Locate the cells, classifying each as a parasitized red blood cell, an uninfected red blood cell, or a white blood cell.
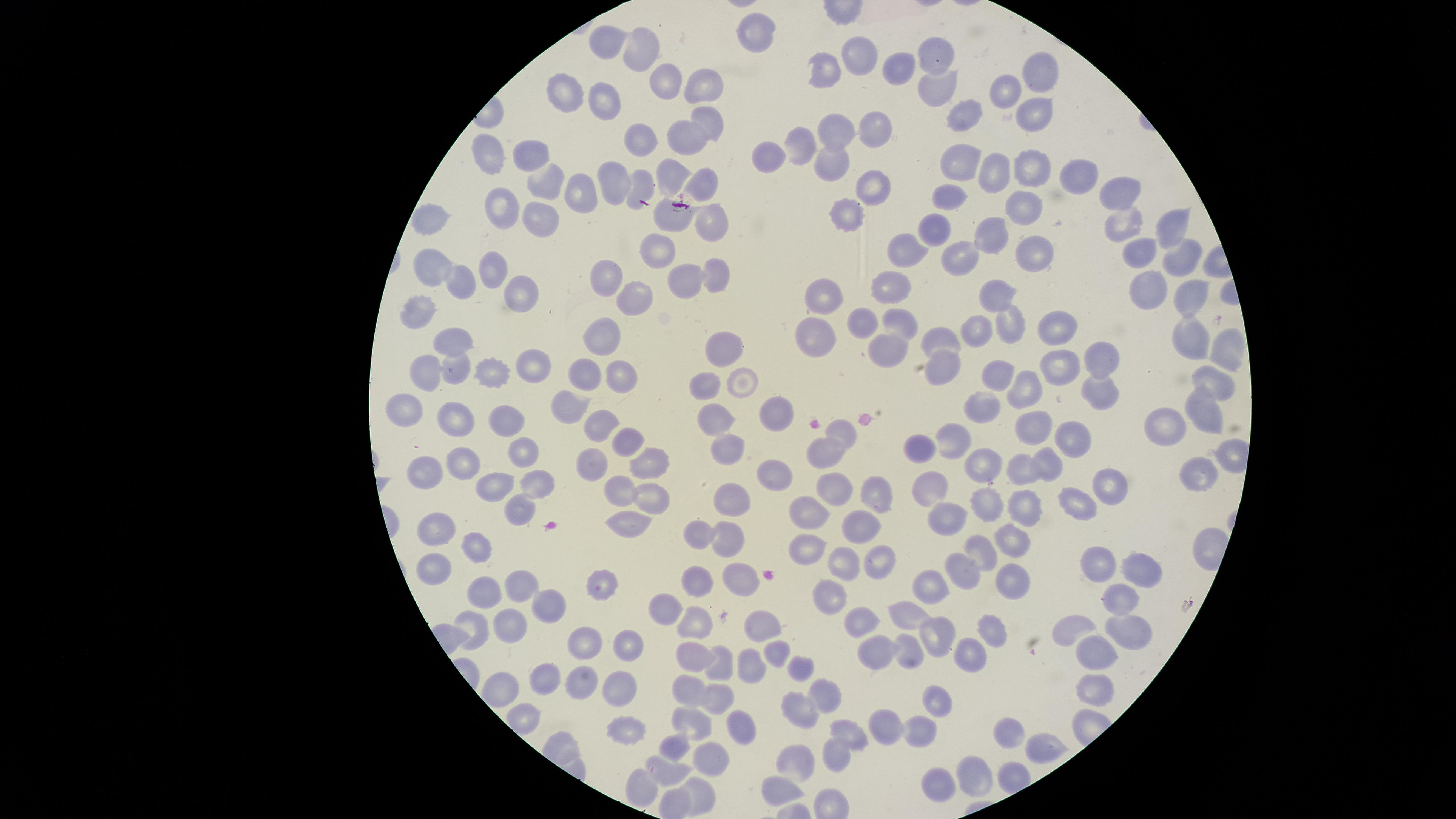
No parasitized red blood cells identified.
Approximate marker points as [x, y] in pixels.
Uninfected red blood cells: [756, 32], [607, 42], [639, 52], [856, 55], [933, 59], [893, 68], [827, 70], [1039, 74], [667, 79], [705, 82], [937, 92], [567, 93], [1003, 93], [599, 105], [1030, 108], [961, 114], [706, 120], [839, 129], [874, 130], [688, 135], [642, 136], [804, 144], [772, 153], [493, 157], [831, 158], [965, 158], [535, 159], [1028, 167], [992, 171], [1071, 172], [618, 174], [672, 174], [547, 184], [702, 184], [873, 184], [639, 185], [1114, 191], [950, 193], [580, 194], [504, 205], [1021, 207], [672, 216], [849, 216], [705, 220], [430, 222], [1123, 222], [541, 224], [1163, 225], [932, 228], [992, 233], [661, 247], [1035, 250], [910, 252], [1142, 253], [959, 259], [1182, 259], [437, 270], [495, 272], [608, 274], [710, 276], [680, 282], [893, 284], [465, 287], [1151, 287], [519, 291], [825, 297], [990, 298], [1187, 298], [636, 302], [421, 315], [866, 322], [902, 322], [1004, 323], [1054, 328], [979, 329], [819, 333], [942, 334], [602, 336], [1193, 338], [448, 340], [720, 342], [1222, 347], [887, 350], [533, 364], [947, 364], [1103, 364], [1053, 365], [452, 368], [426, 371], [622, 374], [490, 375], [582, 375], [996, 376], [1215, 378], [706, 384], [747, 385], [1024, 393], [1099, 394], [984, 399], [569, 406], [411, 409], [1202, 412], [781, 413], [456, 416], [512, 419], [1040, 423], [719, 424], [603, 427], [1165, 427], [844, 429], [626, 436], [1071, 436], [955, 438], [918, 444], [727, 447], [823, 448], [522, 456], [654, 458], [1047, 461], [463, 464], [588, 464], [980, 466], [1025, 469], [1200, 469], [425, 470], [768, 477], [534, 481], [835, 485], [934, 486], [502, 488], [622, 491], [1104, 491], [730, 493], [876, 494], [981, 498], [645, 499], [1024, 503], [1071, 503], [803, 511], [517, 514], [949, 523], [861, 524], [705, 526], [631, 527], [430, 530], [730, 535], [1014, 539], [472, 546], [981, 548], [809, 549], [845, 555], [883, 556], [1099, 561], [1139, 568], [439, 569], [960, 569], [738, 574], [1012, 575], [695, 581], [931, 582], [606, 584], [525, 589], [489, 594], [827, 594], [1119, 599], [666, 605], [548, 607], [912, 614], [864, 617], [759, 622], [475, 624], [694, 624], [1079, 627], [510, 630], [987, 631], [1130, 631], [942, 634], [589, 639], [629, 645], [908, 648], [876, 649], [698, 651], [780, 651], [1098, 652], [969, 655], [723, 662], [747, 662], [800, 664], [580, 678], [545, 679], [624, 685], [686, 685], [505, 691], [1096, 691], [826, 692], [712, 698], [934, 702], [799, 708], [519, 714], [696, 722], [742, 723], [624, 725], [882, 727], [914, 732], [852, 734], [1010, 735], [680, 744], [1049, 744], [838, 755], [711, 761], [798, 764], [669, 768], [977, 779], [938, 787], [639, 789], [779, 793], [700, 799].
No white blood cells identified.

preparation = thin blood smear
visible region = circular
capture = smartphone photograph through the microscope eyepiece
image size = 1456×819 pixels
field of view = single
stain = Giemsa